Give the preparation type.
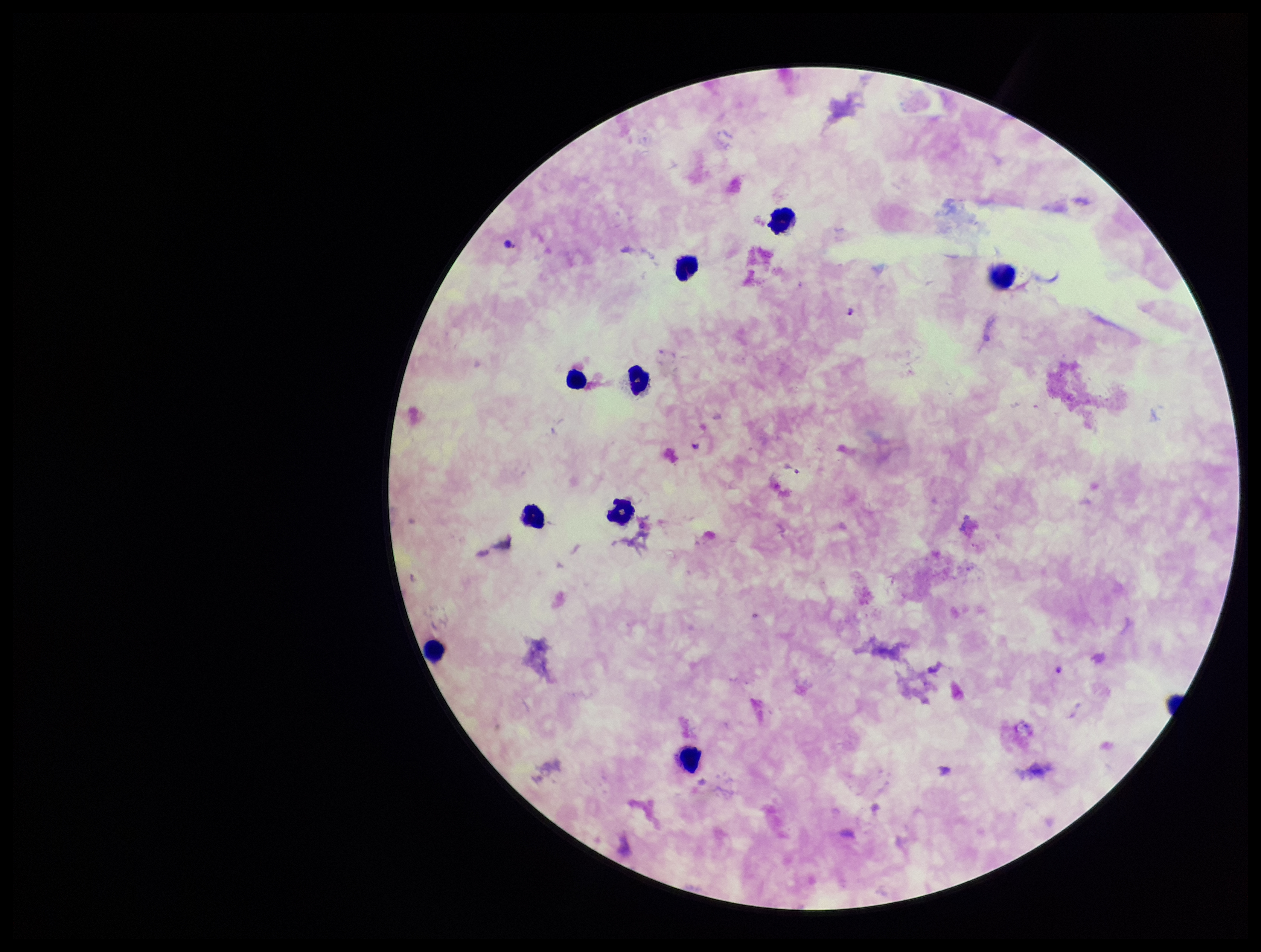

It is a thick blood smear.

Parasite count: 0. Species reported for this patient: Plasmodium falciparum. One field from this slide. Image is 1261×952 pixels. Photographed through the microscope eyepiece with a smartphone camera. Leukocyte count: 10. Stained with Giemsa. Plasmodium parasites: none seen. Patient malaria status: infected.